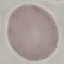

Summary:
  - Result: no malaria parasites seen
  - Preparation: thin smear
  - Capture: smartphone camera at the microscope eyepiece
  - Stain: Giemsa
  - Image type: automatically extracted cell patch, resized to 64 × 64 pixels